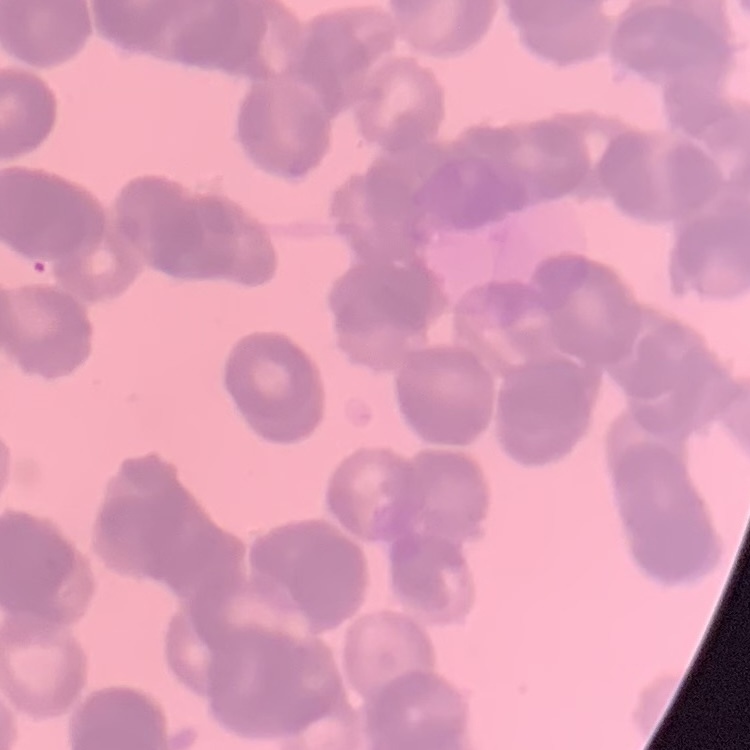

The red blood cells exhibit rouleaux formation. Thin blood film. One tile cut from a larger photomicrograph. Stained with either Field's or Giemsa.